Identify the blood parasite species.
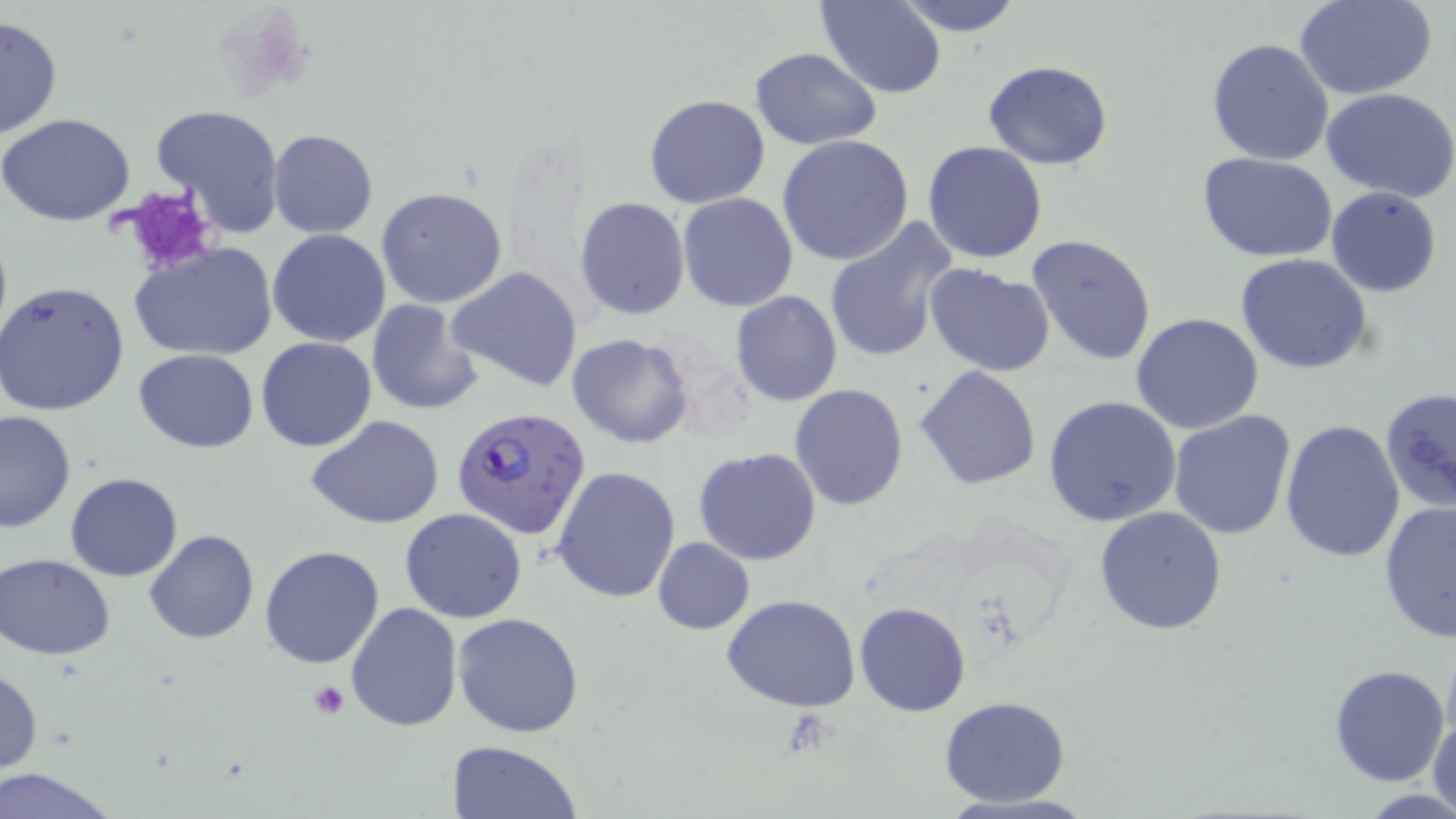

Plasmodium falciparum.

Summary:
  - Coordinate format: approximate bounding boxes as (x1,y1)-(x2,y2) corner pairs in pixels
  - Platelet locations: (117,188)-(219,275), (309,680)-(350,719)
  - Uninfected red blood cell locations: (818,0)-(947,98), (892,0)-(1024,36), (1296,1)-(1437,98), (0,16)-(62,139), (1205,38)-(1335,167), (751,48)-(880,148), (982,59)-(1112,168), (1323,88)-(1456,202), (644,94)-(770,209), (149,104)-(287,237), (0,113)-(135,225), (268,129)-(377,238), (777,135)-(914,266), (922,141)-(1049,263), (1197,152)-(1339,261), (376,187)-(508,309), (1326,187)-(1443,297), (677,193)-(798,311), (574,197)-(689,320), (824,220)-(957,364), (267,229)-(392,347), (1027,234)-(1158,364), (129,241)-(277,362), (1235,253)-(1374,374), (925,265)-(1057,379), (448,266)-(584,392), (0,280)-(130,416), (729,291)-(843,407), (365,299)-(481,416), (1130,313)-(1263,434), (567,333)-(694,449), (257,338)-(377,452), (134,348)-(259,452), (914,366)-(1041,490), (788,384)-(910,511), (1378,387)-(1456,513), (1044,395)-(1181,526), (0,410)-(76,532), (1168,410)-(1297,541), (308,417)-(444,530), (1278,418)-(1405,563), (693,447)-(823,565), (552,465)-(680,602), (64,471)-(182,581), (1378,500)-(1456,642), (1094,505)-(1228,633), (400,509)-(528,623), (143,530)-(260,645), (652,537)-(755,634), (259,543)-(386,667), (1,554)-(116,659), (722,592)-(863,713), (855,602)-(971,717), (345,603)-(462,733), (453,612)-(586,738), (1330,664)-(1449,785), (0,667)-(43,777), (939,696)-(1071,806), (1428,706)-(1456,816), (448,740)-(583,819), (1,768)-(120,819)
  - Plasmodium falciparum-infected red blood cell locations: (453,415)-(591,549)
  - Image size: 1456×819 pixels
  - Magnification: 1000x
  - Preparation: thin blood film
  - Stain: May-Grünwald-Giemsa
  - Modality: light microscopy
  - Field of view: one of a larger specimen